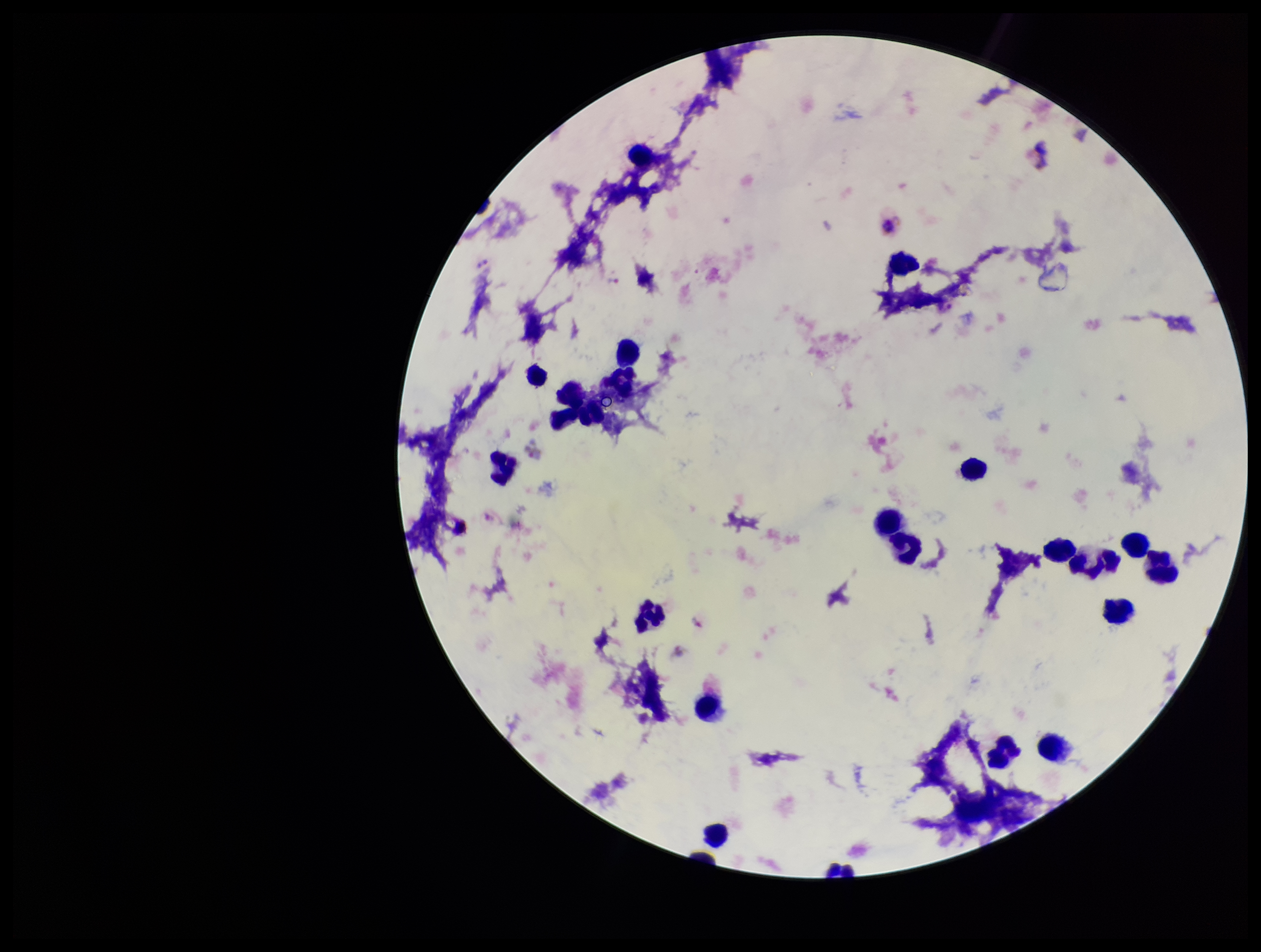

Species reported for this patient: Plasmodium vivax. Parasite count: 4. Stained with Giemsa. Image is 1261×952 pixels. One field from this slide. Patient malaria status: positive. Smartphone photograph taken through the eyepiece of a microscope. Leukocyte count: 24. Preparation: thick. Plasmodium parasites: seen.